Report the malaria status of this cell.
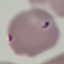
It is uninfected.

Summary:
  - Capture: smartphone through the microscope eyepiece
  - Stain: Giemsa
  - Preparation: thin smear
  - Image type: automatically extracted cell patch, resized to 64 × 64 pixels